Mark where platelets are.
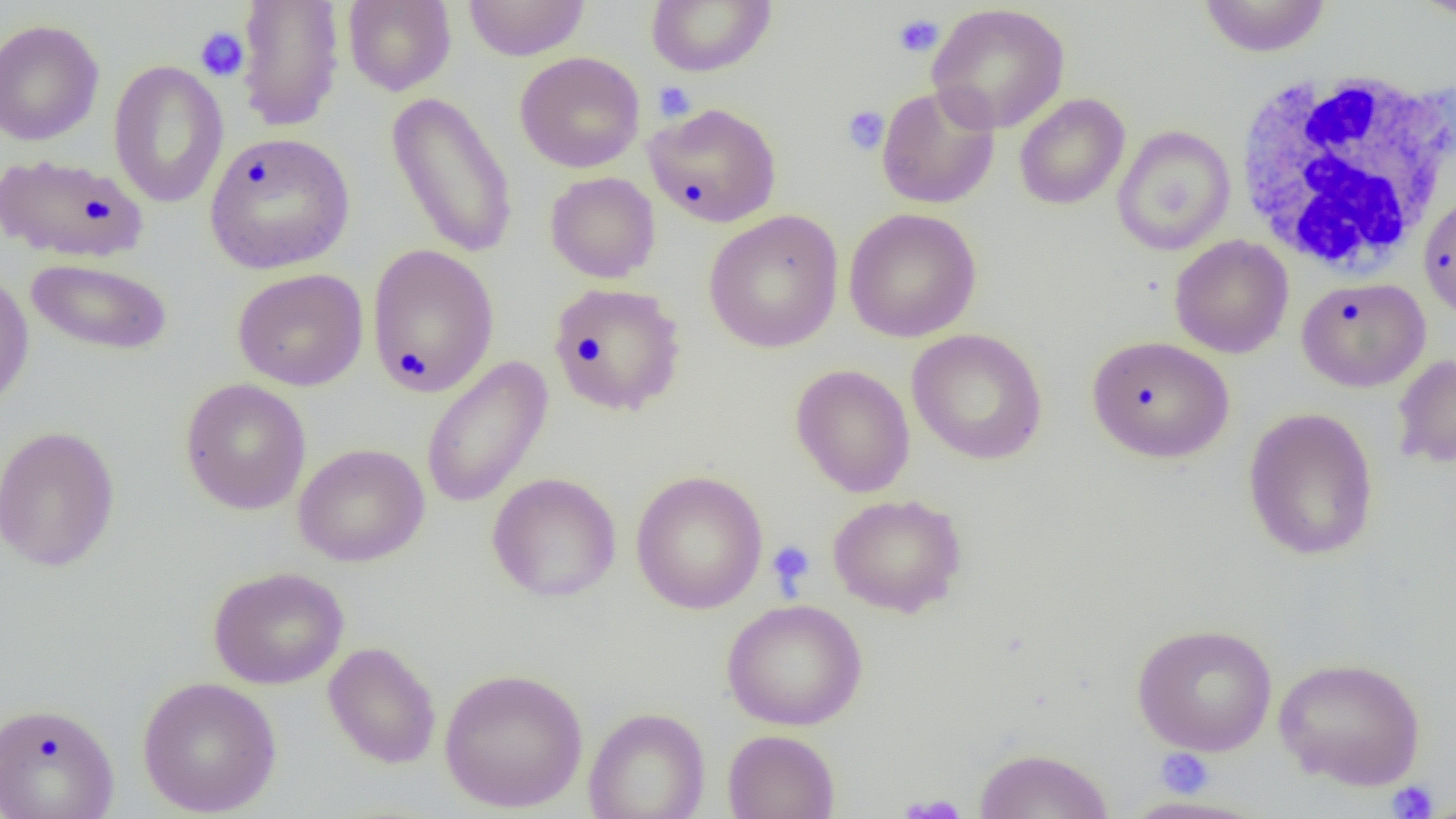
Approximate bounding boxes as named x1/y1/x2/y2 corners in pixels.
Platelets: (x1=893, y1=13, x2=944, y2=58), (x1=194, y1=26, x2=250, y2=82), (x1=652, y1=81, x2=696, y2=122), (x1=842, y1=105, x2=889, y2=156), (x1=767, y1=540, x2=816, y2=594), (x1=1155, y1=747, x2=1214, y2=798), (x1=1386, y1=780, x2=1439, y2=818), (x1=898, y1=794, x2=968, y2=818).

slide-level diagnosis = negative for blood parasites
image size = 1456×819 pixels
modality = light microscopy
preparation = thin blood smear
uninfected red blood cell locations = approximate bounding boxes as named x1/y1/x2/y2 corners in pixels: (x1=234, y1=0, x2=345, y2=132), (x1=646, y1=0, x2=777, y2=77), (x1=1198, y1=0, x2=1331, y2=57), (x1=1409, y1=0, x2=1456, y2=22), (x1=342, y1=1, x2=456, y2=96), (x1=463, y1=1, x2=590, y2=61), (x1=927, y1=3, x2=1070, y2=134), (x1=0, y1=18, x2=105, y2=146), (x1=515, y1=51, x2=645, y2=173), (x1=108, y1=59, x2=229, y2=208), (x1=876, y1=84, x2=1000, y2=209), (x1=385, y1=91, x2=519, y2=260), (x1=1014, y1=93, x2=1130, y2=210), (x1=644, y1=102, x2=782, y2=228), (x1=1112, y1=125, x2=1235, y2=256), (x1=204, y1=132, x2=355, y2=275), (x1=1, y1=154, x2=149, y2=264), (x1=545, y1=172, x2=660, y2=283), (x1=1418, y1=191, x2=1456, y2=320), (x1=843, y1=208, x2=982, y2=342), (x1=704, y1=210, x2=844, y2=354), (x1=1170, y1=235, x2=1294, y2=358), (x1=367, y1=243, x2=500, y2=398), (x1=25, y1=257, x2=173, y2=356), (x1=232, y1=268, x2=369, y2=391), (x1=0, y1=271, x2=34, y2=410), (x1=1297, y1=276, x2=1431, y2=392), (x1=548, y1=281, x2=686, y2=416), (x1=907, y1=328, x2=1048, y2=465), (x1=1086, y1=335, x2=1235, y2=463), (x1=1392, y1=353, x2=1456, y2=471), (x1=420, y1=355, x2=554, y2=510), (x1=790, y1=363, x2=915, y2=498), (x1=179, y1=378, x2=311, y2=515), (x1=1243, y1=407, x2=1380, y2=562), (x1=0, y1=425, x2=121, y2=572), (x1=293, y1=443, x2=430, y2=567), (x1=630, y1=469, x2=768, y2=614), (x1=487, y1=472, x2=621, y2=602), (x1=827, y1=493, x2=966, y2=617), (x1=208, y1=566, x2=349, y2=689), (x1=722, y1=599, x2=868, y2=731), (x1=1132, y1=623, x2=1278, y2=756), (x1=322, y1=641, x2=441, y2=769), (x1=1273, y1=657, x2=1425, y2=790), (x1=439, y1=667, x2=588, y2=813), (x1=137, y1=676, x2=282, y2=817), (x1=0, y1=701, x2=120, y2=819), (x1=584, y1=707, x2=710, y2=819), (x1=723, y1=729, x2=840, y2=818), (x1=973, y1=747, x2=1114, y2=818), (x1=1115, y1=795, x2=1273, y2=818)
white blood cell locations = approximate bounding boxes as named x1/y1/x2/y2 corners in pixels: (x1=1234, y1=69, x2=1455, y2=276)
field of view = one of a larger specimen
magnification = 1000x